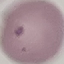

malaria status = uninfected
capture = smartphone camera at the microscope eyepiece
stain = Giemsa
image type = cell patch, automatically extracted from a larger field of view and resized to 64 × 64 pixels
preparation = thin blood smear